Classify this cell by malaria status.
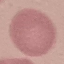
Uninfected.

Summary:
  - Preparation: thin smear
  - Stain: Giemsa
  - Image type: cell patch, automatically extracted from a larger field of view and resized to 64 × 64 pixels
  - Capture: smartphone through the microscope eyepiece